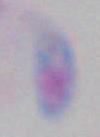
Photomicrograph. Toxoplasma gondii is seen. Captured at 1000x magnification.